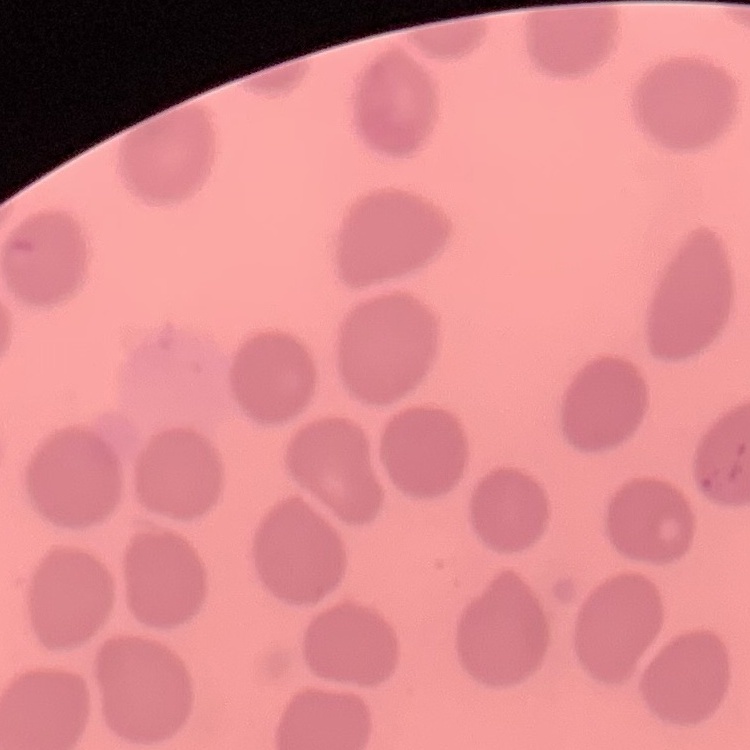

The red blood cells show no rouleaux formation. Square crop of a larger photomicrograph. Stained with either Field's or Giemsa. Thin blood smear.